Assess for Plasmodium parasites.
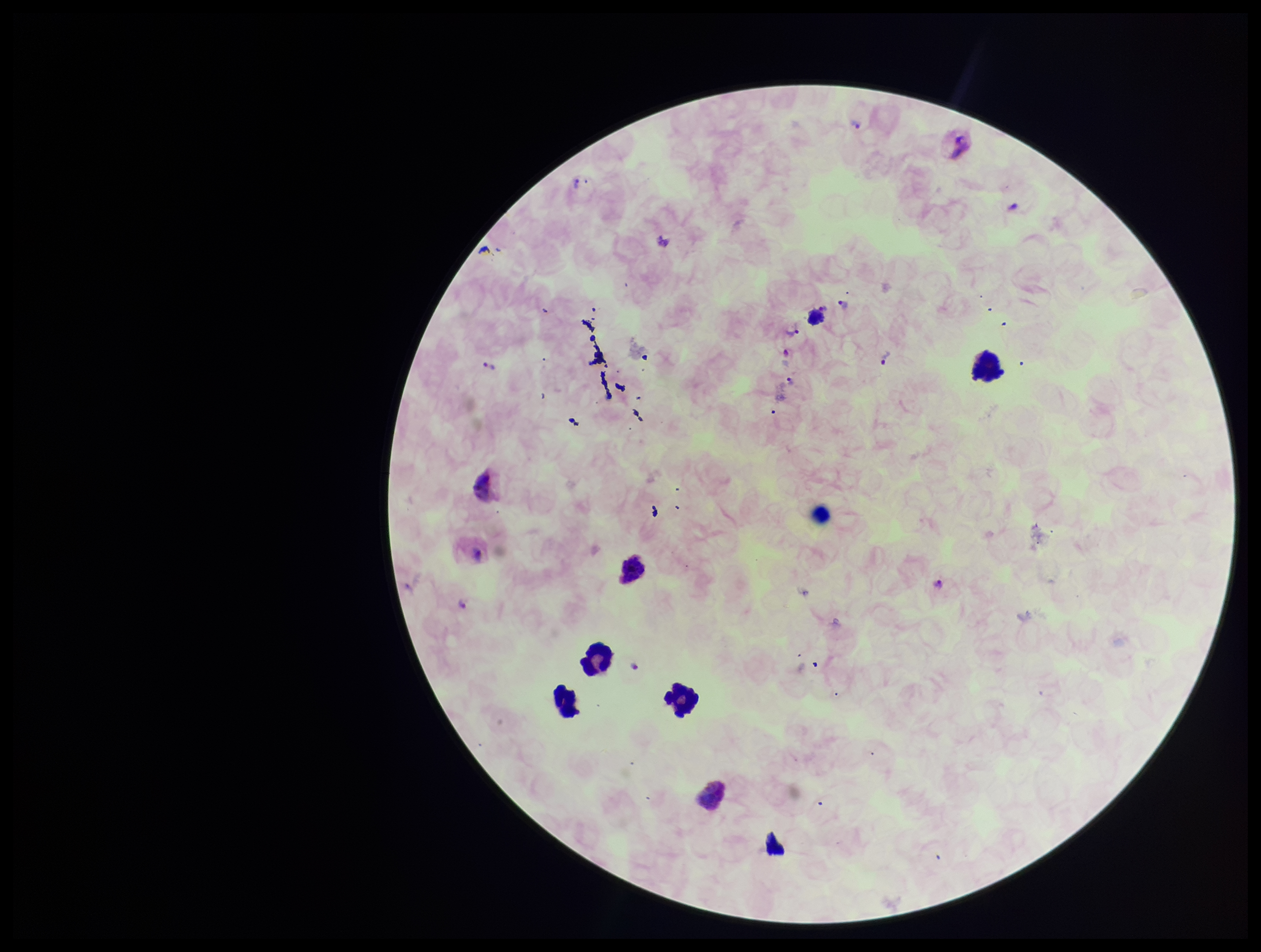

Identified.

preparation = thick smear
capture = smartphone photograph through the microscope eyepiece
image size = 1261×952 pixels
field of view = single
stain = Giemsa
parasite count = 7
patient malaria status = infected
leukocyte count = 5
species reported for this patient = Plasmodium vivax